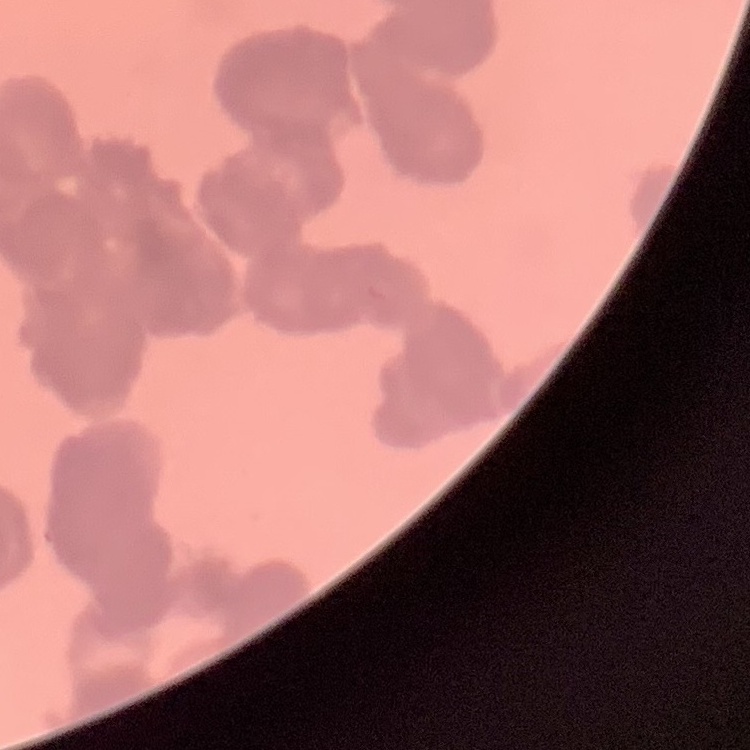

erythrocyte morphology = rouleaux formation
stain = Field's or Giemsa
preparation = thin blood film
image type = one tile cut from a larger photomicrograph